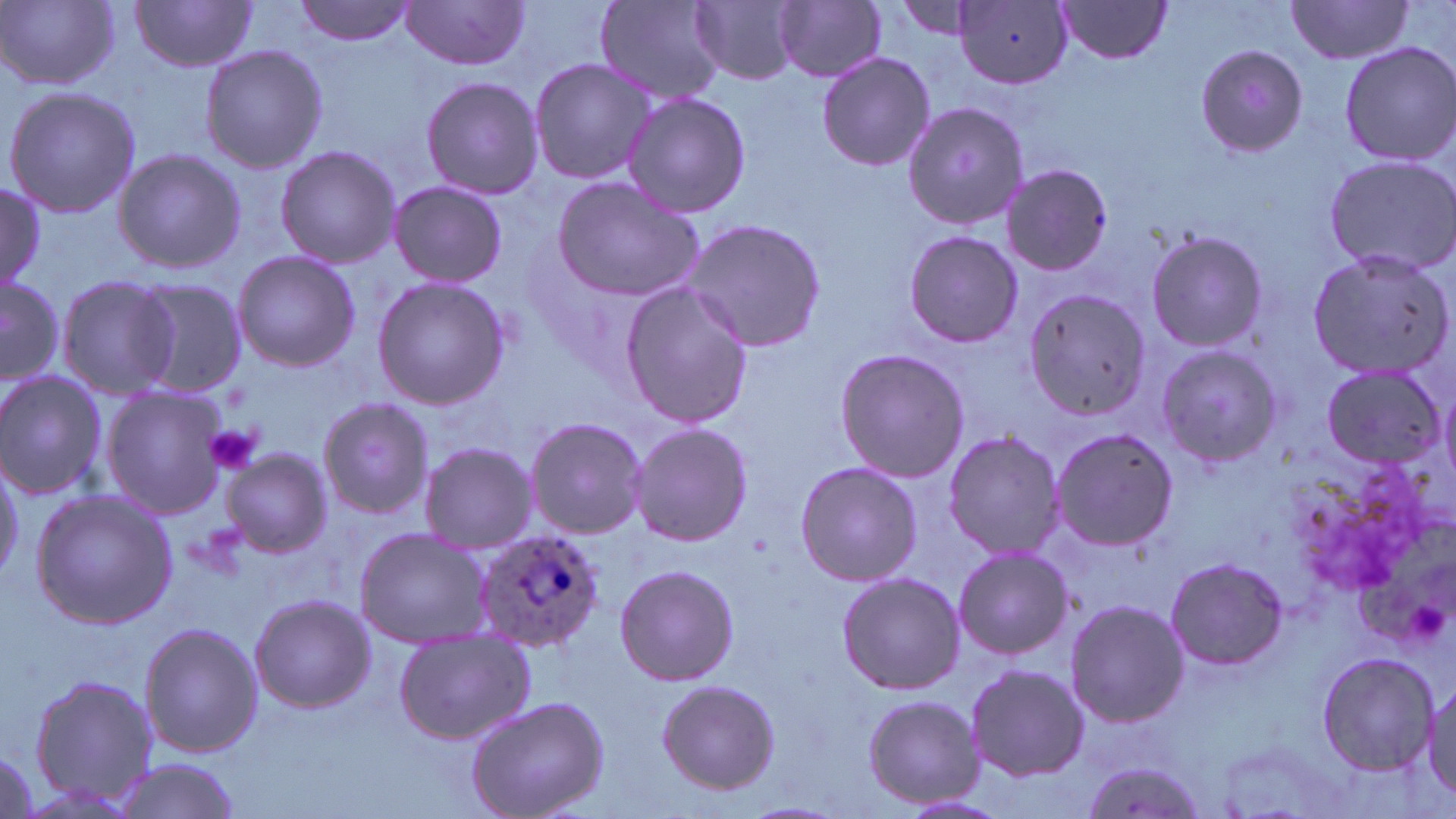 Approximate bounding boxes as named x1/y1/x2/y2 corners in pixels. Platelet locations: (x1=205, y1=426, x2=261, y2=476). Uninfected red blood cell locations: (x1=293, y1=0, x2=416, y2=46), (x1=596, y1=0, x2=727, y2=103), (x1=691, y1=0, x2=802, y2=86), (x1=889, y1=0, x2=988, y2=40), (x1=2, y1=1, x2=119, y2=91), (x1=131, y1=1, x2=261, y2=72), (x1=400, y1=1, x2=532, y2=71), (x1=1053, y1=1, x2=1174, y2=64), (x1=773, y1=2, x2=887, y2=83), (x1=955, y1=2, x2=1076, y2=89), (x1=1284, y1=2, x2=1417, y2=64), (x1=1338, y1=41, x2=1456, y2=167), (x1=199, y1=42, x2=329, y2=175), (x1=1193, y1=43, x2=1309, y2=157), (x1=816, y1=53, x2=936, y2=172), (x1=527, y1=57, x2=656, y2=186), (x1=419, y1=77, x2=545, y2=201), (x1=2, y1=86, x2=143, y2=219), (x1=620, y1=93, x2=752, y2=216), (x1=902, y1=102, x2=1028, y2=231), (x1=274, y1=144, x2=402, y2=269), (x1=112, y1=146, x2=244, y2=274), (x1=1321, y1=154, x2=1456, y2=276), (x1=1000, y1=164, x2=1114, y2=278), (x1=551, y1=174, x2=705, y2=302), (x1=387, y1=181, x2=509, y2=287), (x1=0, y1=183, x2=45, y2=294), (x1=682, y1=217, x2=828, y2=354), (x1=1144, y1=229, x2=1269, y2=354), (x1=902, y1=230, x2=1023, y2=349), (x1=1304, y1=248, x2=1454, y2=382), (x1=231, y1=250, x2=362, y2=372), (x1=0, y1=271, x2=66, y2=385), (x1=56, y1=275, x2=182, y2=397), (x1=372, y1=277, x2=511, y2=409), (x1=132, y1=279, x2=247, y2=396), (x1=618, y1=281, x2=754, y2=428), (x1=1021, y1=290, x2=1150, y2=422), (x1=1154, y1=342, x2=1282, y2=466), (x1=834, y1=348, x2=969, y2=482), (x1=1319, y1=366, x2=1449, y2=470), (x1=0, y1=369, x2=111, y2=502), (x1=1435, y1=379, x2=1456, y2=492), (x1=99, y1=385, x2=228, y2=519), (x1=316, y1=395, x2=436, y2=521), (x1=523, y1=416, x2=648, y2=539), (x1=630, y1=424, x2=752, y2=548), (x1=1048, y1=426, x2=1180, y2=552), (x1=941, y1=430, x2=1064, y2=560), (x1=418, y1=441, x2=536, y2=554), (x1=221, y1=448, x2=332, y2=559), (x1=0, y1=456, x2=25, y2=583), (x1=794, y1=462, x2=921, y2=587), (x1=28, y1=488, x2=178, y2=630), (x1=352, y1=527, x2=490, y2=647), (x1=952, y1=546, x2=1073, y2=660), (x1=1164, y1=555, x2=1288, y2=671), (x1=613, y1=564, x2=739, y2=686), (x1=836, y1=571, x2=964, y2=695), (x1=248, y1=595, x2=376, y2=715), (x1=1064, y1=599, x2=1189, y2=728), (x1=138, y1=621, x2=262, y2=760), (x1=393, y1=626, x2=535, y2=746), (x1=1316, y1=651, x2=1438, y2=774), (x1=965, y1=663, x2=1089, y2=781), (x1=27, y1=672, x2=157, y2=813), (x1=656, y1=679, x2=780, y2=793), (x1=1423, y1=682, x2=1456, y2=804), (x1=862, y1=694, x2=985, y2=810), (x1=465, y1=696, x2=609, y2=819), (x1=1079, y1=754, x2=1210, y2=819), (x1=107, y1=757, x2=244, y2=819), (x1=902, y1=794, x2=1008, y2=816), (x1=739, y1=800, x2=848, y2=818). Plasmodium ovale-infected red blood cell locations: (x1=472, y1=528, x2=604, y2=652). Slide-level diagnosis: Plasmodium ovale. Image is 1456×819 pixels. May-Grünwald-Giemsa stain. One field of a larger specimen. Thin blood film. Optical microscopy. 1000x magnification.